Classify this cell by malaria status.
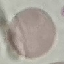

Uninfected.

Summary:
  - Image type: cell patch, automatically extracted from a larger field of view and resized to 64 × 64 pixels
  - Stain: Giemsa
  - Capture: smartphone camera at the microscope eyepiece
  - Preparation: thin blood smear